Assess this cell for malaria.
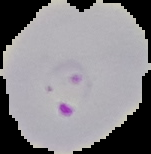

It is parasitized.

{
  "preparation": "thin blood film",
  "image_type": "segmented cell region on a black background",
  "image_size": "151×154 pixels"
}